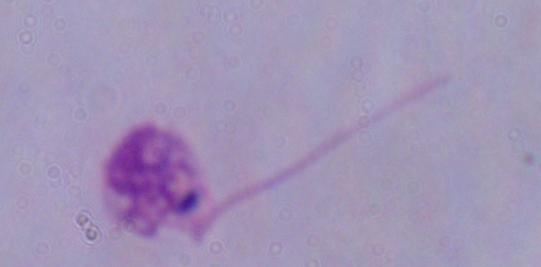

Captured at 1000x magnification. Photomicrograph. A Leishmania parasite is seen.